Classify this cell by malaria status.
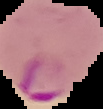

It is parasitized.

Summary:
  - Image size: 103×109 pixels
  - Preparation: thin blood film
  - Image type: segmented cell region on a black background